Name the parasite shown.
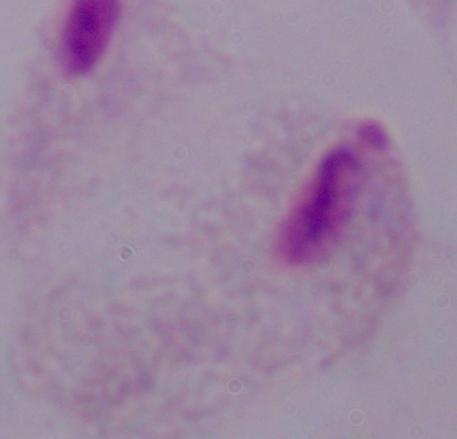

A trichomonad.

magnification = 1000x
modality = photomicrograph